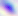

Summary:
  - Identification: Toxoplasma gondii
  - Modality: micrograph
  - Magnification: 400x